State which parasite is depicted.
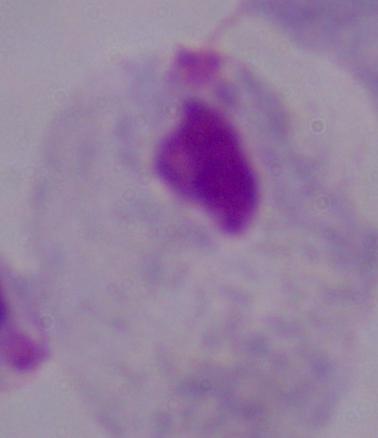
A trichomonad.

Photomicrograph. Captured at 1000x magnification.